Name the blood parasite species.
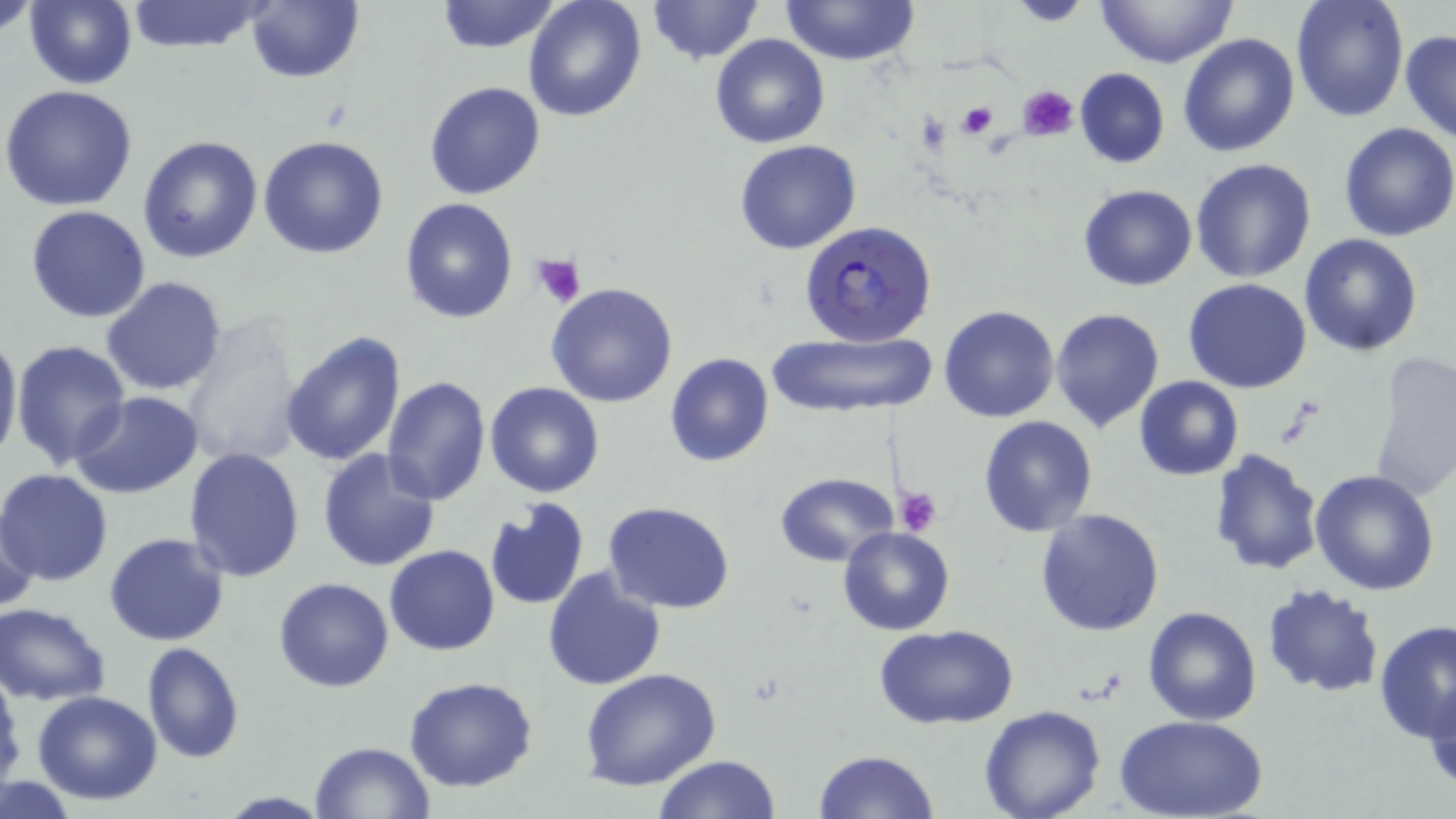

Plasmodium falciparum.

Approximate bounding boxes as (x1,y1)-(x2,y2) corner pairs in pixels. Plasmodium falciparum-infected red blood cell locations: (799,221)-(936,346). Uninfected red blood cell locations: (1,0)-(41,40), (25,0)-(137,89), (123,0)-(273,53), (435,0)-(563,53), (522,0)-(648,123), (646,0)-(764,64), (1096,0)-(1238,68), (1290,0)-(1409,122), (780,1)-(918,66), (1001,1)-(1094,26), (244,2)-(364,83), (1401,31)-(1456,143), (1178,32)-(1300,157), (709,33)-(830,149), (1074,67)-(1169,169), (424,81)-(546,200), (1,86)-(139,212), (1338,122)-(1456,241), (138,135)-(264,264), (258,135)-(390,259), (734,139)-(862,255), (1190,158)-(1317,283), (1077,183)-(1197,291), (399,199)-(519,323), (24,205)-(151,322), (1298,234)-(1422,355), (100,277)-(227,396), (1183,278)-(1312,393), (545,281)-(679,408), (939,305)-(1059,422), (1050,308)-(1164,432), (178,318)-(305,469), (0,327)-(22,469), (279,329)-(408,468), (765,331)-(937,415), (9,338)-(130,472), (665,353)-(774,469), (1368,353)-(1456,503), (381,374)-(491,505), (1134,375)-(1244,480), (484,383)-(605,499), (70,392)-(202,497), (978,414)-(1100,537), (184,447)-(305,582), (316,448)-(441,572), (1208,449)-(1323,576), (0,468)-(115,585), (1309,469)-(1440,594), (774,472)-(898,566), (483,500)-(589,612), (604,501)-(735,614), (1,505)-(40,616), (1036,508)-(1165,635), (837,526)-(956,637), (104,532)-(230,647), (383,545)-(500,655), (542,566)-(667,690), (274,577)-(395,692), (1261,581)-(1385,700), (1,603)-(114,704), (1141,605)-(1262,724), (1376,619)-(1456,744), (875,624)-(1021,730), (141,642)-(245,764), (0,666)-(24,794), (579,670)-(721,792), (403,677)-(538,792), (1425,678)-(1456,795), (31,691)-(163,805), (979,705)-(1107,819), (1118,714)-(1265,819), (308,741)-(436,818), (813,750)-(939,819), (653,754)-(783,818), (0,777)-(80,818), (215,791)-(332,819). Platelet locations: (1020,85)-(1078,140), (955,101)-(999,139), (531,252)-(587,307), (894,486)-(942,537). May-Grünwald-Giemsa-stained preparation. Image is 1456×819 pixels. Thin blood film. 1000x magnification. Light microscopy. One field of a larger specimen.